Outline each blood parasite and name the species.
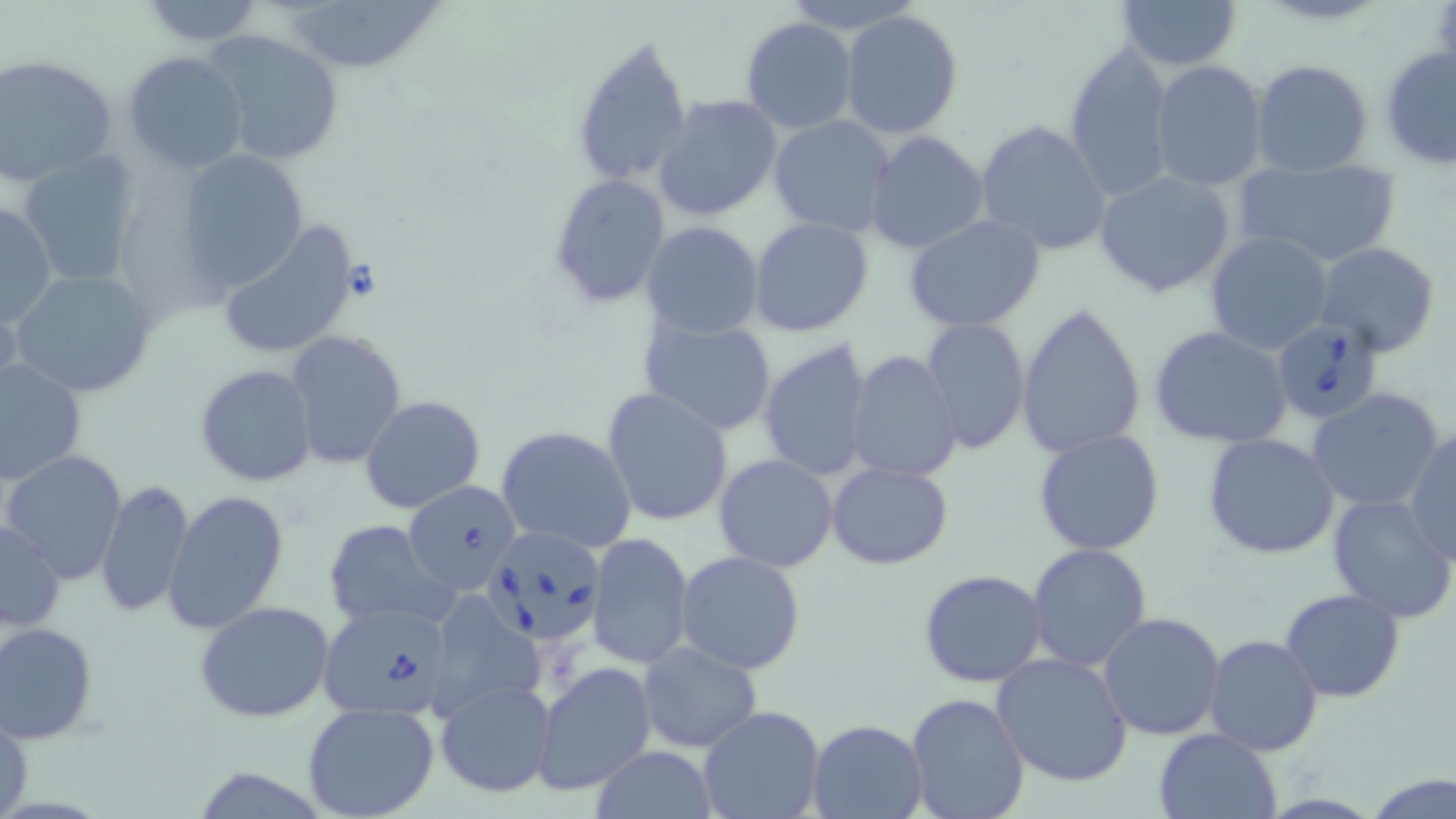
Approximate bounding boxes as (x1,y1)-(x2,y2) corner pairs in pixels.
Babesia divergens-infected red blood cells: (1271,316)-(1390,425), (402,479)-(522,593), (490,533)-(605,643), (319,604)-(451,723).
No Plasmodium falciparum, Plasmodium ovale, Plasmodium malariae, Plasmodium vivax, or Trypanosoma brucei observed.

Uninfected red blood cell locations: (135,0)-(267,47), (278,0)-(448,72), (778,0)-(925,35), (1116,0)-(1243,72), (839,9)-(963,139), (740,18)-(858,135), (202,28)-(344,167), (571,32)-(692,189), (1062,42)-(1174,199), (1380,46)-(1456,169), (122,50)-(249,174), (1,53)-(121,186), (1150,59)-(1268,191), (1250,59)-(1374,178), (651,94)-(784,224), (769,115)-(895,238), (974,119)-(1112,258), (865,130)-(989,254), (17,149)-(144,289), (176,150)-(311,292), (1232,154)-(1402,269), (1094,169)-(1238,300), (546,174)-(669,307), (0,200)-(57,327), (904,214)-(1046,332), (749,217)-(874,336), (640,219)-(764,338), (214,220)-(362,361), (1205,231)-(1334,355), (1313,242)-(1441,357), (9,268)-(157,399), (1017,303)-(1147,459), (639,312)-(778,436), (919,318)-(1030,454), (1150,325)-(1293,449), (285,331)-(408,470), (758,338)-(877,481), (846,351)-(961,483), (1,358)-(86,485), (194,364)-(318,487), (601,387)-(734,526), (1306,388)-(1446,514), (360,395)-(487,515), (496,425)-(638,554), (1406,426)-(1455,560), (1033,428)-(1166,555), (1202,434)-(1341,561), (2,450)-(129,584), (714,454)-(838,571), (826,461)-(953,569), (96,477)-(192,619), (162,490)-(290,634), (1327,492)-(1456,625), (1,518)-(66,633), (323,519)-(456,631), (587,533)-(695,669), (1026,542)-(1152,671), (675,551)-(807,674), (918,569)-(1047,687), (1280,589)-(1405,702), (437,595)-(548,721), (192,600)-(337,722), (1096,612)-(1226,742), (0,621)-(99,744), (1205,634)-(1324,756), (637,642)-(762,751), (990,653)-(1134,790), (533,662)-(656,796), (435,675)-(556,799), (905,692)-(1030,819), (301,701)-(441,819), (1,705)-(31,818), (696,706)-(826,819), (808,719)-(929,818), (1155,728)-(1280,817), (588,746)-(718,819), (1368,774)-(1456,818). Slide-level diagnosis: Babesia divergens. May-Grünwald-Giemsa-stained preparation. Light microscopy. Thin blood smear. One field of a larger specimen. 1000x magnification. Image is 1456×819 pixels.